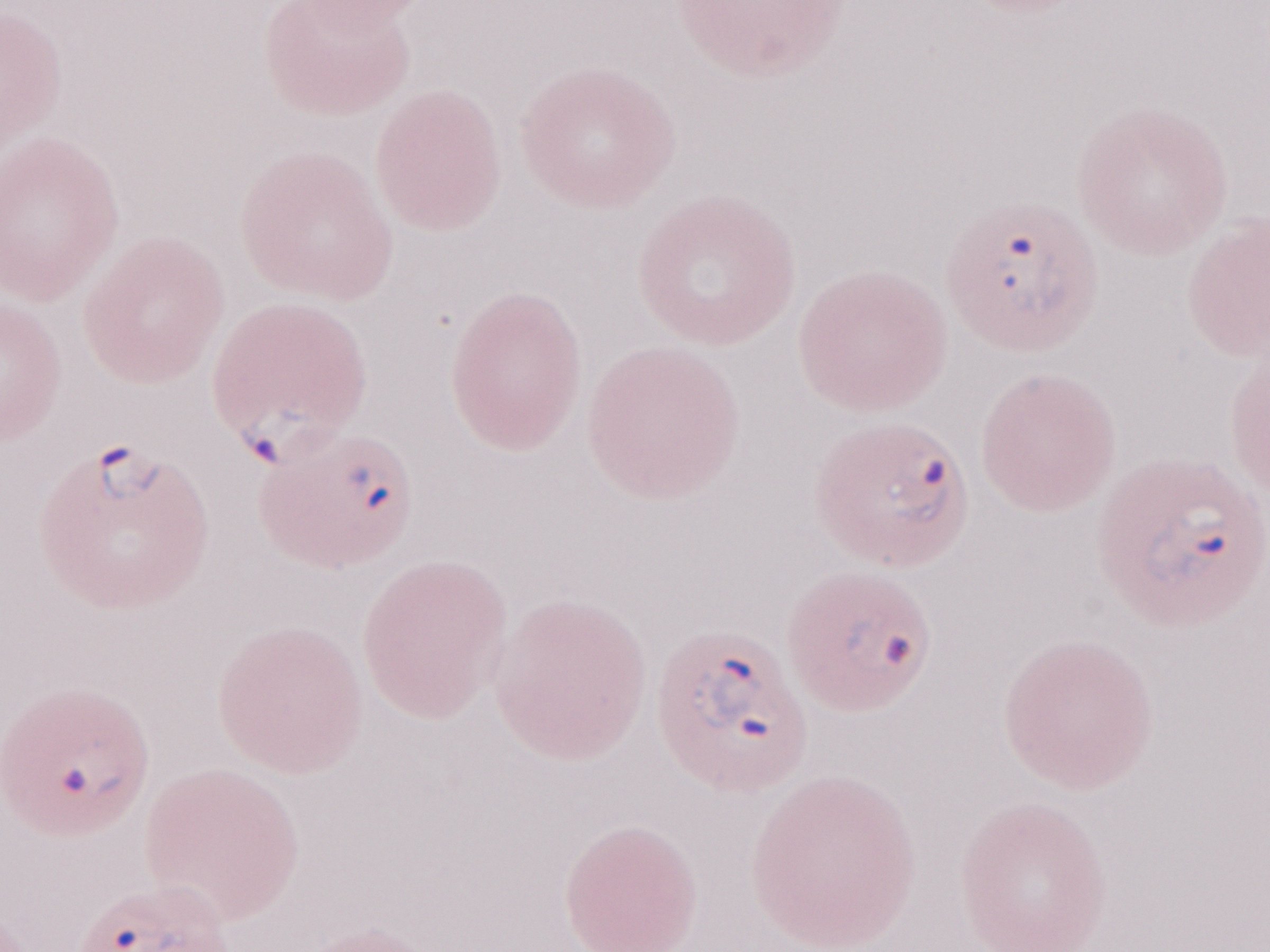 1,000x magnification. May-Grünwald-Giemsa (MGG) stain. One field of this slide. Olympus BX43 microscope and DP73 digital camera. Patient diagnosis: malaria infection. Thin peripheral-blood smear. Image is 1270×952 pixels.